Locate and identify every blood parasite.
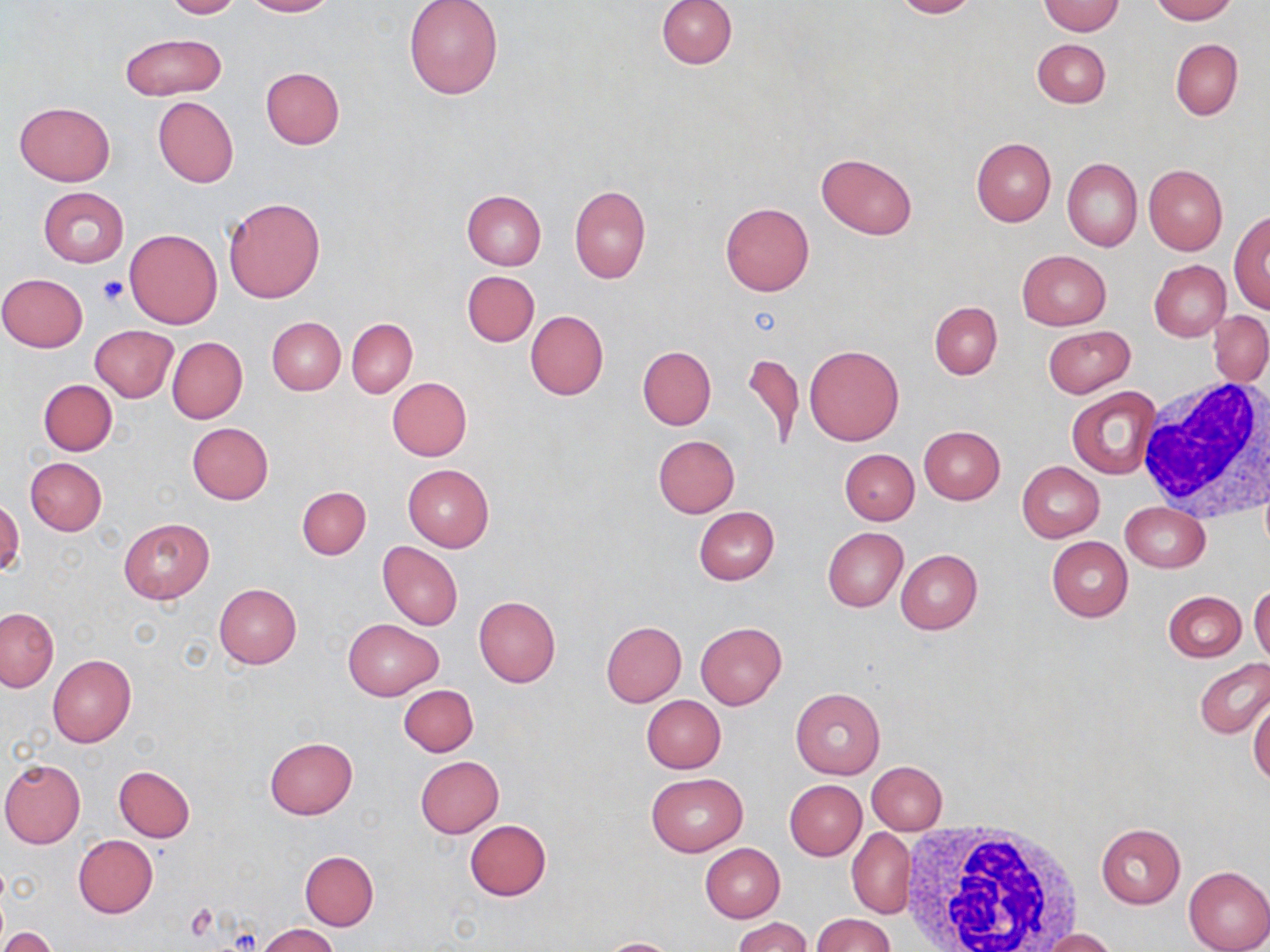
No blood parasites observed.

Approximate bounding boxes as [x1, y1, x2, y2] in pixels. Uninfected red blood cell locations: [161, 0, 242, 19], [243, 0, 335, 17], [656, 0, 736, 69], [892, 0, 980, 19], [1150, 0, 1235, 23], [404, 1, 503, 101], [1038, 1, 1124, 36], [120, 32, 224, 100], [1170, 38, 1242, 120], [1032, 39, 1110, 108], [260, 66, 345, 148], [153, 97, 239, 187], [15, 102, 114, 185], [971, 138, 1055, 225], [815, 153, 917, 239], [1062, 157, 1142, 252], [1144, 164, 1227, 254], [570, 186, 650, 284], [38, 187, 129, 266], [462, 190, 546, 270], [223, 197, 326, 304], [720, 203, 814, 296], [1230, 211, 1270, 312], [124, 229, 223, 329], [1017, 249, 1111, 329], [1149, 260, 1231, 342], [463, 270, 539, 347], [0, 274, 87, 352], [930, 301, 1001, 378], [525, 310, 609, 399], [1208, 310, 1270, 386], [266, 316, 345, 395], [346, 318, 417, 398], [90, 325, 178, 401], [1042, 326, 1135, 397], [168, 337, 247, 423], [804, 344, 904, 445], [638, 345, 716, 429], [744, 351, 804, 450], [386, 376, 472, 460], [38, 378, 117, 456], [1066, 387, 1163, 480], [187, 422, 273, 504], [918, 426, 1005, 504], [653, 435, 739, 517], [840, 449, 919, 525], [25, 457, 107, 535], [1017, 462, 1104, 541], [402, 464, 493, 552], [297, 485, 371, 560], [0, 499, 25, 576], [1119, 502, 1209, 572], [693, 505, 779, 585], [118, 517, 214, 603], [822, 528, 907, 611], [1046, 536, 1133, 621], [378, 542, 462, 630], [896, 550, 982, 634], [213, 583, 302, 669], [1249, 584, 1270, 666], [1163, 591, 1246, 662], [473, 595, 561, 687], [1, 608, 58, 692], [343, 619, 442, 700], [601, 621, 686, 706], [696, 622, 787, 709], [48, 654, 137, 748], [1195, 660, 1270, 738], [399, 685, 478, 756], [790, 687, 885, 779], [641, 695, 726, 773], [1248, 696, 1270, 785], [264, 737, 358, 820], [415, 755, 503, 837], [0, 759, 85, 848], [867, 761, 947, 833], [113, 766, 195, 842], [645, 773, 747, 856], [784, 780, 867, 860], [465, 820, 551, 901], [1095, 823, 1185, 909], [846, 828, 915, 919], [73, 835, 157, 918], [699, 843, 784, 922], [300, 851, 378, 931], [1182, 865, 1270, 952], [812, 914, 896, 952], [732, 917, 810, 952], [257, 924, 340, 952], [1043, 928, 1118, 951], [2, 929, 60, 952], [597, 938, 682, 952]. White blood cell locations: [1136, 376, 1270, 523], [896, 817, 1083, 952]. Platelet locations: [98, 276, 129, 305]. Slide-level diagnosis: negative for blood parasites. May-Grünwald-Giemsa stain. Thin blood film. Image is 1270×952 pixels. Single field of view. Light microscopy. 1000x magnification.